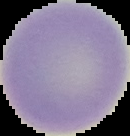
Summary:
  - Result: negative for Plasmodium parasites
  - Preparation: thin blood film
  - Image type: segmented cell region with the area outside set to black
  - Image size: 130×136 pixels